Assess this cell for malaria.
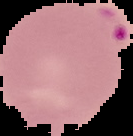

Parasitized.

image size = 133×136 pixels
image type = cell region segmented out of the field of view; surrounding area masked to black
preparation = thin blood smear